Identify the parasite.
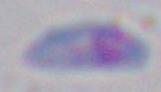

Toxoplasma gondii.

modality = micrograph
magnification = 1000x